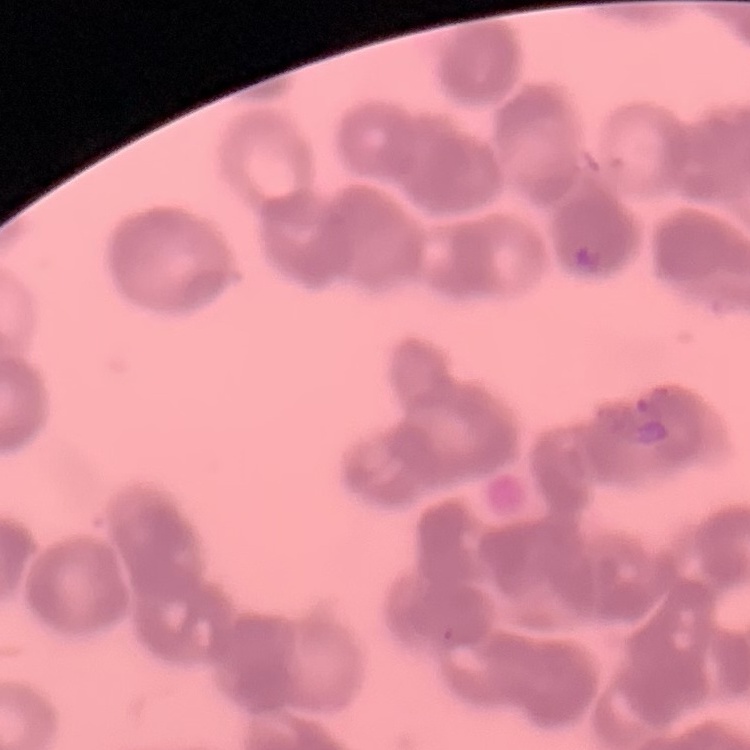 The red blood cells show rouleaux formation. Stained with either Field's or Giemsa. Thin peripheral smear. One tile cut from a larger photomicrograph.